State which parasite is depicted.
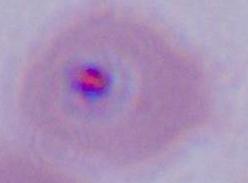
Plasmodium.

Captured at either 400x or 1000x magnification. Photomicrograph.